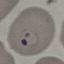

malaria status = parasitized
stain = Giemsa
image type = automatically extracted cell patch, resized to 64 × 64 pixels
capture = smartphone through the microscope eyepiece
preparation = thin blood smear